State which cell type is depicted.
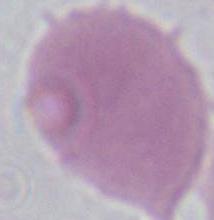
This is an erythrocyte.

Summary:
  - Magnification: 1000x
  - Modality: micrograph